Report the malaria status of this cell.
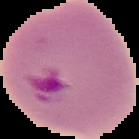

Parasitized.

Summary:
  - Image type: segmented cell region on a black background
  - Image size: 139×139 pixels
  - Preparation: thin blood film